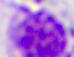

{
  "magnification": "400x",
  "modality": "micrograph",
  "identification": "leukocyte"
}